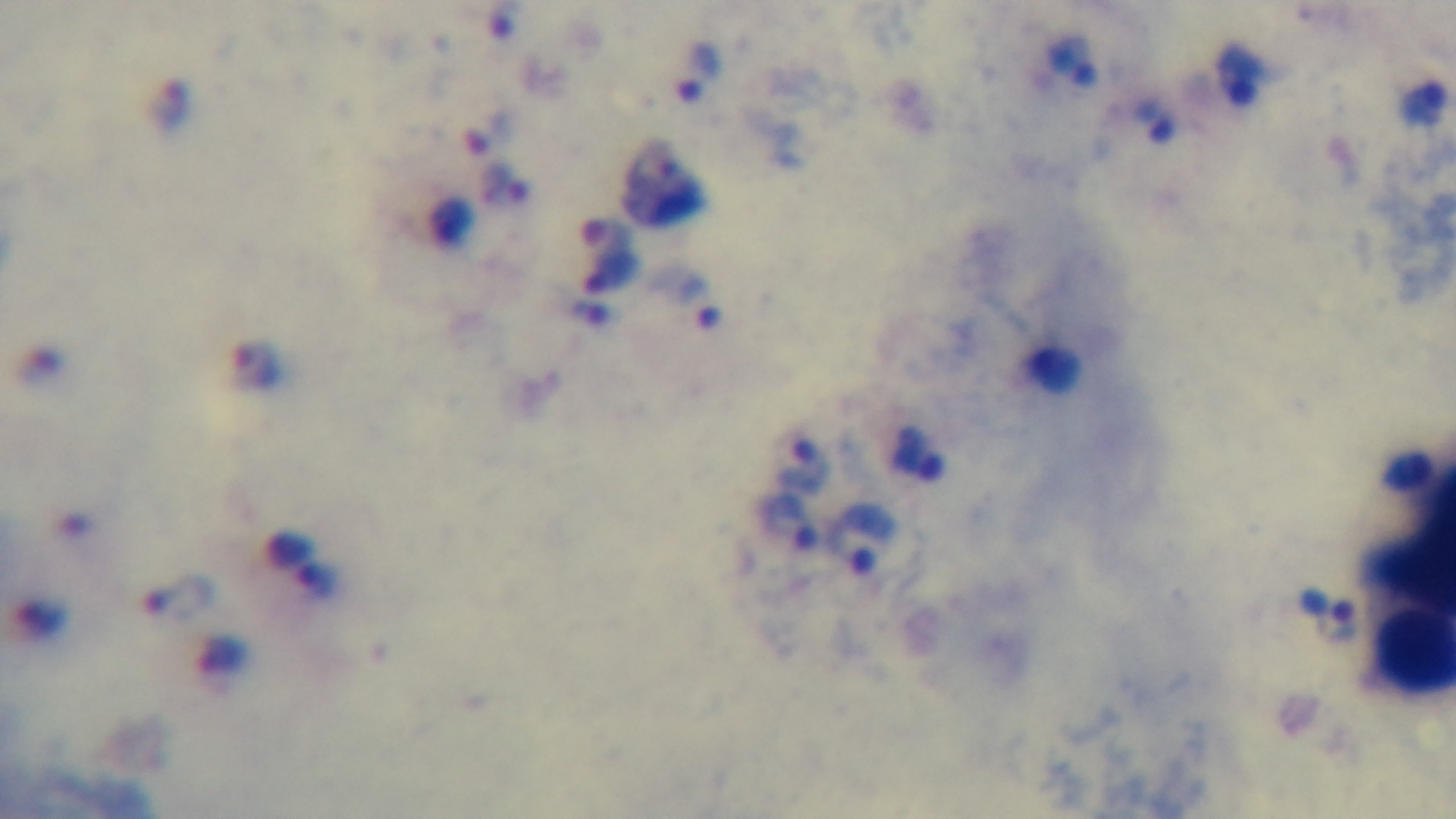
objective: 100x oil immersion
malaria_status: positive
field_of_view: one from the slide
stain: Giemsa
modality: light microscopy
preparation: thick blood film
capture: mounted 4K digital camera